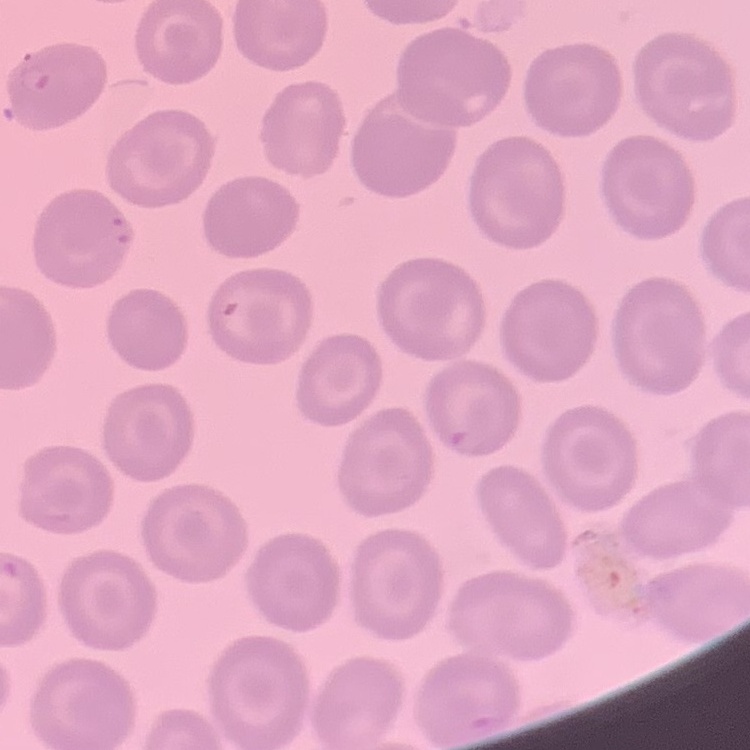

Summary:
  - Red blood cell morphology: no rouleaux formation
  - Preparation: thin blood film
  - Image type: one tile cut from a larger photomicrograph
  - Stain: Field's or Giemsa